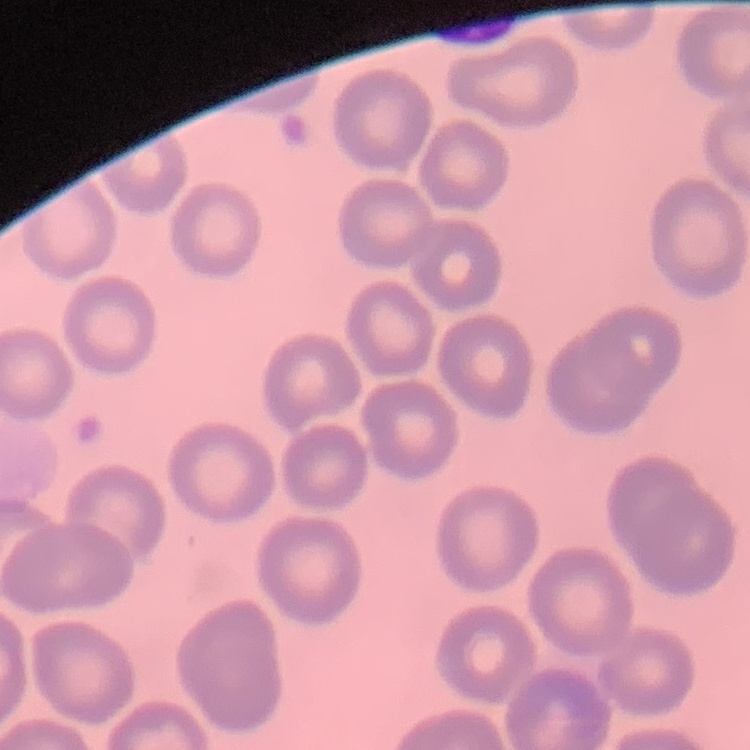
Summary:
  - Erythrocyte morphology: no rouleaux formation
  - Preparation: thin blood film
  - Image type: square crop of a larger photomicrograph
  - Stain: Field's or Giemsa